Report the malaria status of this cell.
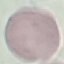
Uninfected.

{
  "stain": "Giemsa",
  "image_type": "cell patch, automatically extracted from a larger field of view and resized to 64 × 64 pixels",
  "preparation": "thin blood smear",
  "capture": "smartphone camera at the microscope eyepiece"
}